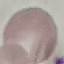
result: negative for malaria parasites
preparation: thin blood smear
stain: Giemsa
capture: smartphone camera at the microscope eyepiece
image_type: automatically extracted cell patch, resized to 64 × 64 pixels